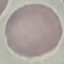
Result: no malaria parasites seen. Giemsa stain. Thin blood smear. Automatically extracted cell patch, resized to 64 × 64 pixels. Acquired by smartphone through the microscope eyepiece.